Comment on the morphology of the erythrocytes.
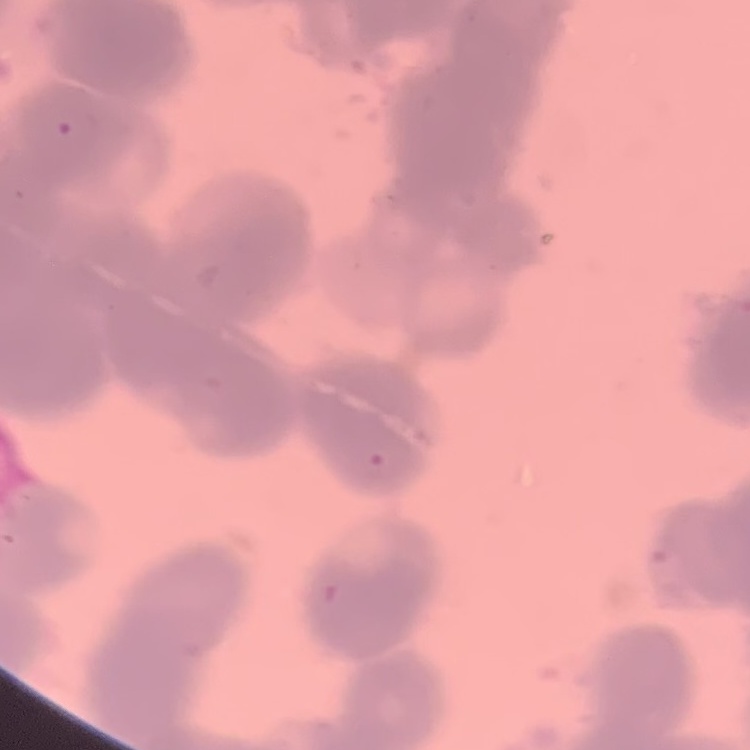
Rouleaux formation.

preparation: thin blood smear
image_type: one tile cut from a larger photomicrograph
stain: Field's or Giemsa